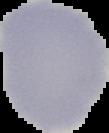
preparation = thin blood smear
image type = segmented cell region on a black background
malaria status = uninfected
image size = 109×133 pixels